Report the malaria status of this cell.
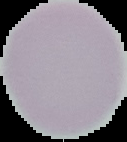
It is uninfected.

Summary:
  - Image type: segmented cell region with the area outside set to black
  - Preparation: thin blood smear
  - Image size: 127×142 pixels